Assess the morphology of the erythrocytes.
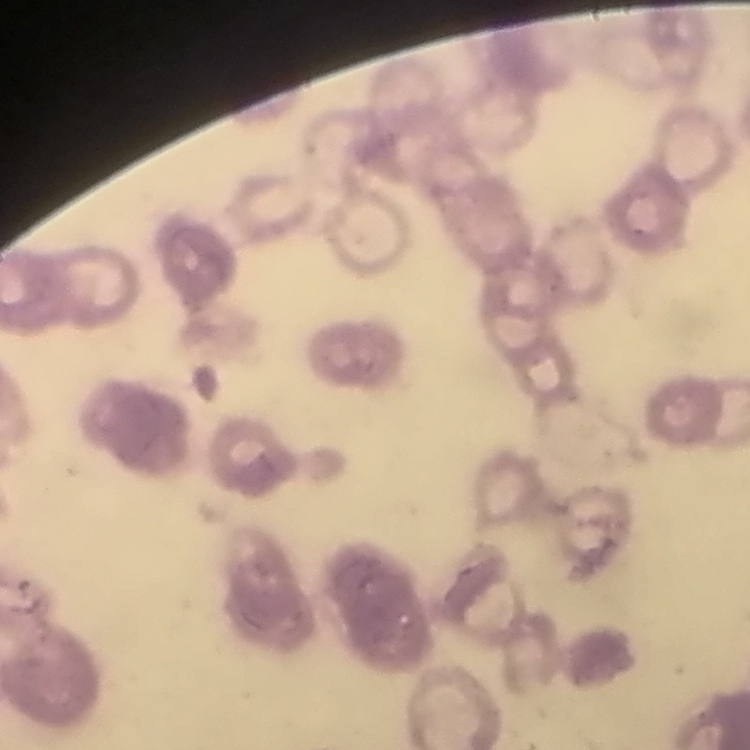

Rouleaux formation.

Summary:
  - Image type: one tile cut from a larger photomicrograph
  - Stain: Field's or Giemsa
  - Preparation: thin peripheral smear